Assess this cell for malaria.
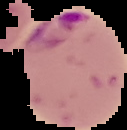

Parasitized.

Image is 127×130 pixels. Cell region segmented out of the field of view; the surrounding area is masked to black. From a thin blood smear.